Identify the blood parasite species.
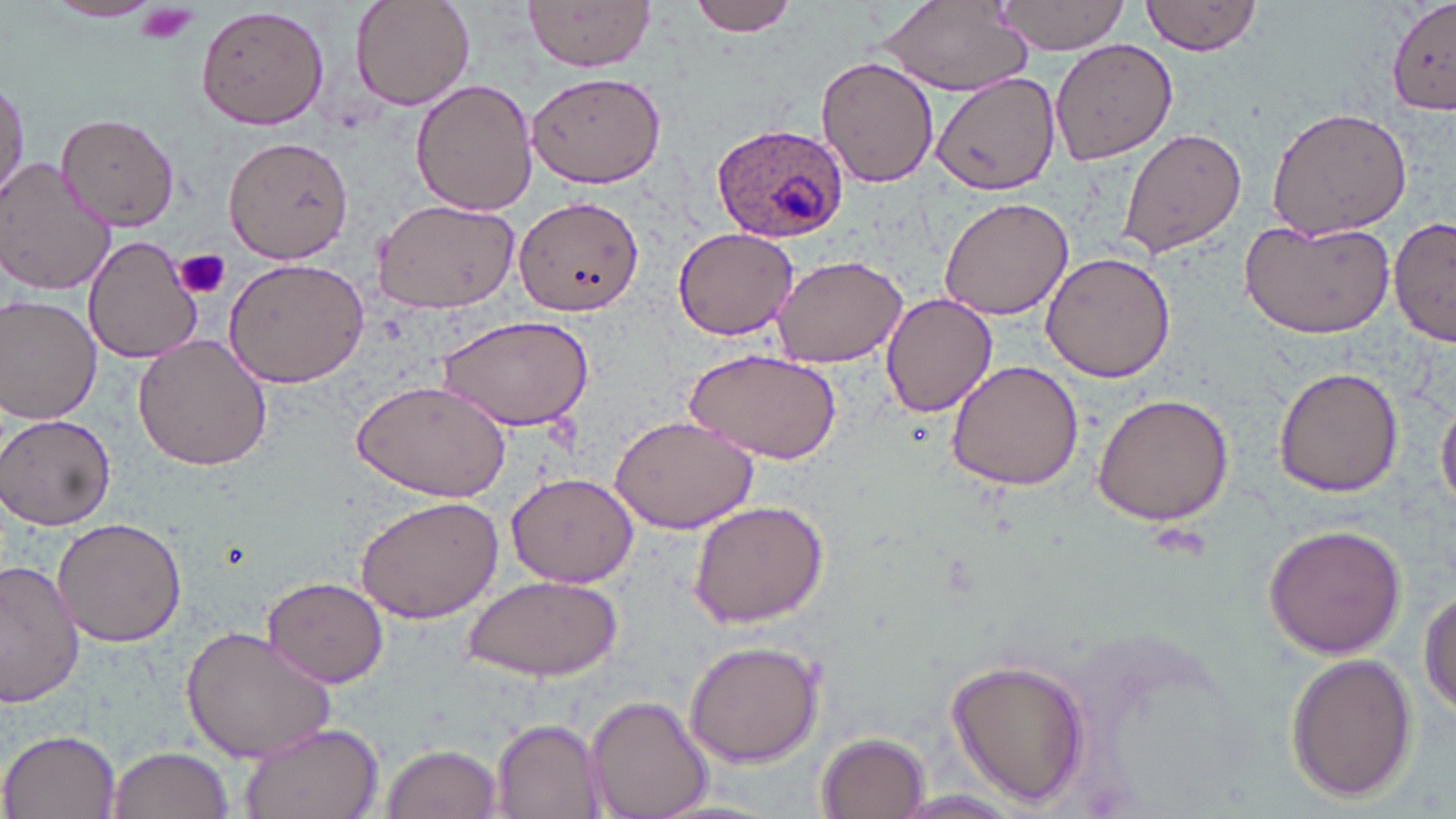
Plasmodium ovale.

stain = May-Grünwald-Giemsa
Plasmodium ovale-infected red blood cell locations = approximate bounding boxes as (x1, y1, x2, y2) in pixels: (711, 122, 848, 243)
preparation = thin blood film
image size = 1456×819 pixels
platelet locations = approximate bounding boxes as (x1, y1, x2, y2) in pixels: (135, 2, 205, 45), (173, 249, 230, 301)
field of view = single
modality = light microscopy
magnification = 1000x
uninfected red blood cell locations = approximate bounding boxes as (x1, y1, x2, y2) in pixels: (348, 0, 475, 110), (525, 0, 657, 72), (687, 0, 801, 36), (990, 1, 1131, 55), (1141, 1, 1264, 56), (43, 2, 163, 24), (879, 2, 1033, 95), (1387, 2, 1456, 114), (196, 3, 331, 131), (1049, 38, 1177, 166), (816, 58, 938, 188), (525, 68, 666, 188), (933, 71, 1060, 194), (0, 78, 29, 205), (412, 79, 540, 216), (1265, 106, 1413, 241), (56, 113, 182, 228), (1119, 126, 1248, 259), (221, 137, 354, 263), (1, 159, 117, 296), (514, 194, 642, 315), (939, 195, 1073, 321), (370, 196, 517, 314), (1389, 215, 1454, 347), (1239, 217, 1395, 339), (672, 226, 801, 341), (83, 234, 201, 362), (1042, 251, 1174, 383), (771, 253, 909, 368), (222, 256, 369, 388), (880, 292, 997, 418), (0, 295, 101, 426), (435, 314, 594, 431), (133, 334, 273, 473), (686, 348, 843, 461), (945, 359, 1083, 492), (1273, 365, 1404, 498), (351, 379, 513, 502), (1090, 392, 1235, 526), (1437, 395, 1456, 512), (609, 412, 760, 534), (2, 414, 119, 532), (507, 472, 639, 587), (354, 493, 507, 625), (687, 498, 830, 628), (52, 518, 187, 646), (1261, 522, 1408, 658), (0, 560, 83, 709), (463, 575, 621, 682), (261, 577, 390, 687), (1418, 585, 1455, 720), (180, 626, 337, 762), (684, 637, 827, 768), (1286, 651, 1418, 803), (945, 657, 1094, 808), (585, 694, 712, 819), (239, 720, 385, 819), (490, 720, 606, 817), (2, 729, 123, 818), (817, 733, 933, 818), (380, 742, 503, 819), (106, 745, 233, 819), (888, 791, 1030, 818)